Give the extent of all Plasmodium ovale-infected red blood cells.
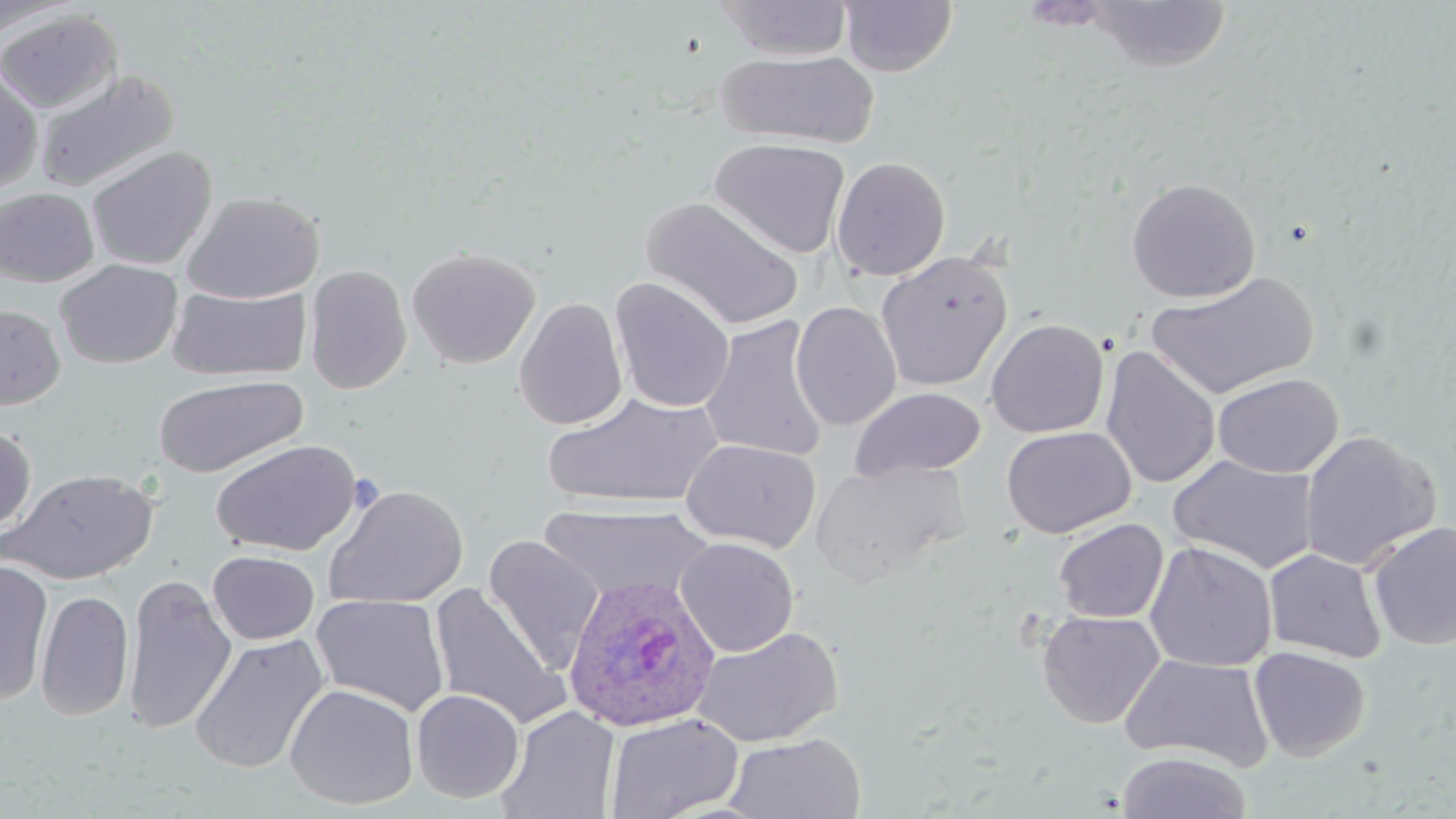
Approximate bounding boxes as (x1, y1, x2, y2) in pixels.
Plasmodium ovale-infected red blood cells: (563, 574, 721, 734).

slide_level_diagnosis: Plasmodium ovale
stain: May-Grünwald-Giemsa
image_size: 1456×819 pixels
preparation: thin blood smear
magnification: 1000x
field_of_view: one of a larger specimen
uninfected_red_blood_cell_locations: 'approximate bounding boxes as (x1, y1, x2, y2) in pixels: (718, 0, 853, 61), (0, 1, 74, 39), (839, 1, 956, 77), (1085, 1, 1234, 72), (0, 10, 123, 115), (717, 50, 878, 148), (0, 64, 43, 195), (34, 69, 179, 193), (710, 137, 850, 259), (86, 146, 217, 271), (831, 156, 950, 281), (1125, 177, 1261, 303), (0, 187, 100, 287), (181, 191, 325, 304), (642, 196, 805, 332), (406, 246, 541, 369), (876, 251, 1013, 391), (55, 259, 183, 369), (304, 264, 412, 394), (1148, 271, 1317, 400), (610, 277, 735, 413), (167, 285, 311, 382), (514, 296, 628, 430), (790, 301, 902, 431), (0, 303, 66, 410), (698, 315, 830, 463), (986, 317, 1109, 439), (1100, 346, 1221, 489), (1212, 372, 1343, 478), (153, 375, 309, 478), (850, 387, 985, 480), (543, 392, 724, 509), (1001, 425, 1136, 538), (0, 426, 37, 537), (1299, 430, 1440, 571), (210, 438, 362, 557), (681, 438, 821, 553), (1168, 454, 1320, 575), (810, 460, 967, 587), (1, 467, 159, 585), (23, 472, 144, 726), (324, 484, 468, 609), (539, 503, 715, 603), (1053, 518, 1168, 623), (1367, 520, 1456, 651), (483, 536, 604, 672), (675, 536, 799, 657), (1144, 541, 1277, 672), (1263, 548, 1387, 664), (208, 551, 320, 645), (0, 558, 54, 705), (123, 574, 236, 734), (427, 584, 569, 729), (35, 590, 134, 721), (311, 593, 450, 717), (1037, 610, 1165, 729), (692, 625, 843, 747), (189, 632, 329, 774), (1249, 646, 1371, 761), (1119, 653, 1274, 771), (284, 683, 419, 810), (411, 689, 525, 803), (497, 705, 620, 819), (605, 712, 744, 819), (723, 732, 866, 819), (1115, 751, 1253, 819)'
modality: light microscopy